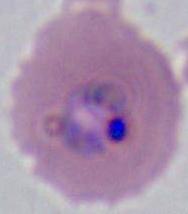

Summary:
  - Modality: micrograph
  - Identification: Plasmodium
  - Magnification: 400x or 1000x